State which parasite is depicted.
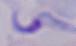
This is a trypanosome.

modality = photomicrograph
magnification = 1000x